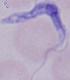
identification: trypanosome
magnification: 1000x
modality: micrograph